Classify this cell by malaria status.
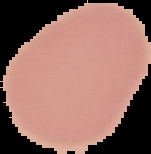
Uninfected.

image_type: segmented cell region with the area outside set to black
image_size: 151×154 pixels
preparation: thin blood film